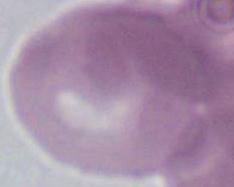

modality: photomicrograph
identification: erythrocyte
magnification: 1000x